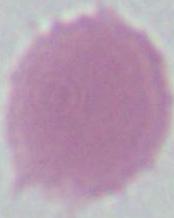
Summary:
  - Modality: photomicrograph
  - Magnification: 1000x
  - Identification: erythrocyte